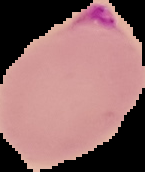
Result: malaria parasites identified. Image is 145×172 pixels. From a thin blood smear. Cell region segmented out of the field of view; the surrounding area is masked to black.